Locate every uninfected red blood cell.
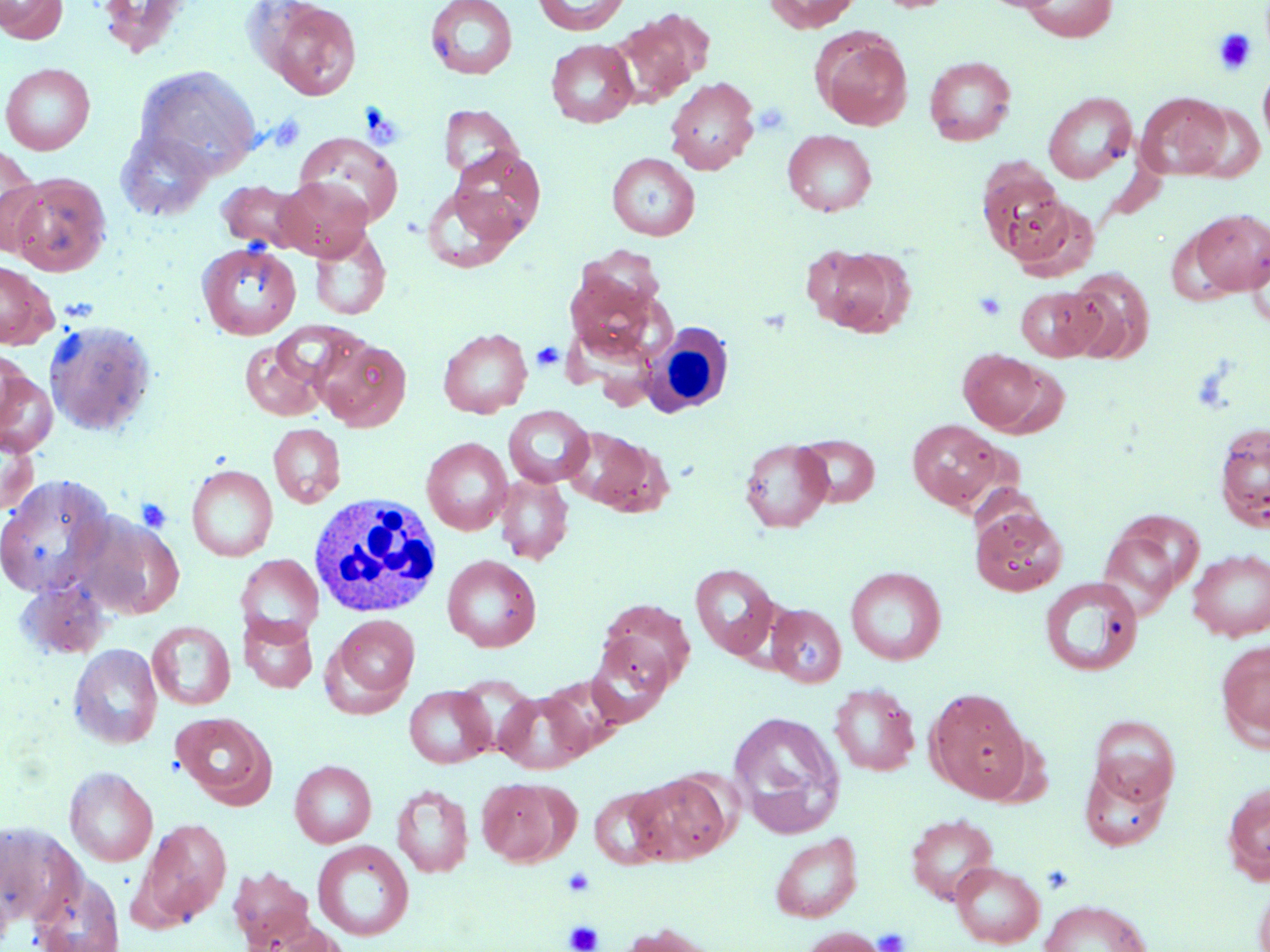
Approximate bounding boxes as (x1, y1, x2, y2) in pixels.
Uninfected red blood cells: (1, 0, 67, 44), (96, 0, 193, 57), (425, 0, 518, 80), (533, 0, 630, 35), (764, 0, 861, 33), (875, 0, 959, 13), (261, 1, 362, 100), (1021, 1, 1118, 42), (613, 12, 706, 106), (813, 30, 913, 130), (546, 39, 638, 128), (924, 56, 1016, 145), (0, 63, 95, 154), (134, 65, 262, 176), (1258, 65, 1270, 148), (665, 77, 759, 174), (1043, 92, 1137, 183), (1136, 92, 1230, 180), (1186, 102, 1268, 182), (439, 105, 523, 182), (782, 130, 877, 216), (117, 131, 216, 221), (293, 132, 403, 227), (0, 143, 45, 254), (450, 148, 546, 241), (607, 153, 700, 240), (976, 157, 1070, 261), (5, 172, 112, 276), (273, 177, 373, 260), (216, 180, 311, 253), (423, 185, 521, 272), (1003, 196, 1099, 280), (1190, 208, 1270, 296), (309, 227, 391, 321), (197, 241, 301, 341), (1247, 241, 1270, 329), (807, 244, 915, 337), (0, 260, 56, 349), (1065, 270, 1154, 364), (564, 271, 673, 372), (1016, 286, 1103, 361), (44, 320, 155, 435), (438, 327, 533, 418), (315, 336, 412, 431), (240, 340, 327, 420), (0, 347, 30, 430), (959, 349, 1049, 435), (0, 369, 58, 457), (503, 405, 594, 487), (907, 419, 1007, 512), (1214, 421, 1270, 531), (268, 423, 346, 508), (561, 427, 662, 513), (0, 428, 38, 520), (797, 434, 880, 507), (422, 437, 513, 535), (740, 439, 833, 532), (187, 465, 278, 561), (495, 473, 574, 564), (0, 474, 116, 600), (970, 506, 1068, 596), (74, 512, 183, 619), (1098, 515, 1201, 617), (1187, 548, 1270, 641), (236, 553, 323, 643), (442, 554, 541, 652), (690, 563, 780, 659), (845, 566, 945, 665), (15, 575, 113, 661), (1039, 578, 1143, 676), (598, 599, 695, 692), (766, 604, 846, 687), (238, 614, 318, 693), (328, 615, 420, 707), (147, 622, 235, 710), (586, 635, 673, 726), (1216, 639, 1270, 749), (69, 644, 162, 749), (539, 676, 626, 755), (829, 684, 920, 776), (404, 685, 494, 769), (495, 689, 592, 774), (927, 689, 1032, 801), (727, 710, 846, 839), (172, 712, 274, 806), (1089, 715, 1180, 805), (290, 760, 376, 848), (1080, 761, 1171, 852), (65, 766, 158, 867), (627, 772, 731, 865), (477, 777, 571, 867), (1222, 782, 1270, 884), (392, 784, 473, 878), (589, 786, 673, 870), (906, 813, 998, 905), (138, 818, 233, 926), (770, 832, 863, 922), (312, 840, 414, 941), (950, 861, 1045, 948), (227, 864, 316, 949), (31, 873, 125, 952), (1253, 874, 1270, 952), (1039, 899, 1152, 952), (241, 913, 347, 951), (617, 923, 721, 952), (798, 926, 888, 952).

{
  "slide_level_diagnosis": "no evidence of blood parasites",
  "stain": "May-Grünwald-Giemsa",
  "white_blood_cell_locations": "approximate bounding boxes as (x1, y1, x2, y2) in pixels: (642, 322, 734, 417), (308, 492, 443, 618)",
  "image_size": "1270×952 pixels",
  "preparation": "thin blood smear",
  "modality": "light microscopy",
  "magnification": "1000x",
  "platelet_locations": "approximate bounding boxes as (x1, y1, x2, y2) in pixels: (1214, 29, 1256, 75), (752, 102, 793, 136), (266, 113, 307, 153), (973, 291, 1007, 321), (531, 341, 565, 372), (1190, 362, 1237, 415), (135, 497, 173, 534), (561, 867, 597, 898), (564, 920, 603, 952), (872, 927, 911, 952)",
  "field_of_view": "single"
}